Identify the cell.
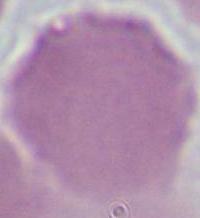
An erythrocyte.

Summary:
  - Modality: micrograph
  - Magnification: 1000x